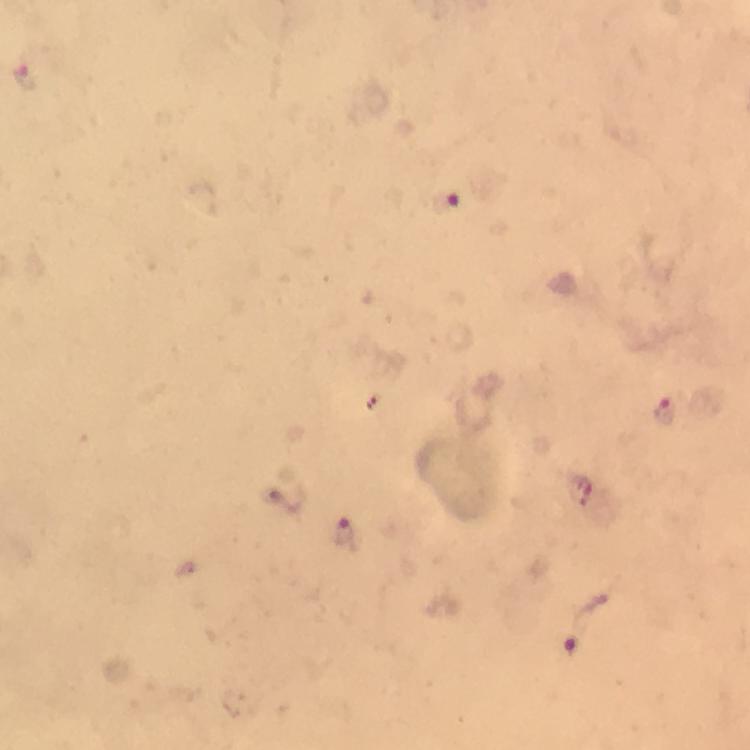
capture = smartphone mounted on the microscope
Plasmodium parasite locations = approximate centers as {x, y} in pixels: {26, 73}, {445, 201}, {666, 411}, {346, 535}, {572, 643}
preparation = thick smear
immersion oil = applied
stain = Giemsa
magnification = 100x
image size = 750×750 pixels
context = from a malaria diagnostic workup
cropped from = a single field of view